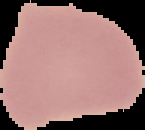
preparation: thin blood film
image_type: cell region segmented out of the field of view; surrounding area masked to black
malaria_status: uninfected
image_size: 145×130 pixels